Report the malaria status of this cell.
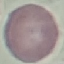

It is uninfected.

preparation: thin blood smear
capture: smartphone through the microscope eyepiece
stain: Giemsa
image_type: cell patch, automatically extracted from a larger field of view and resized to 64 × 64 pixels